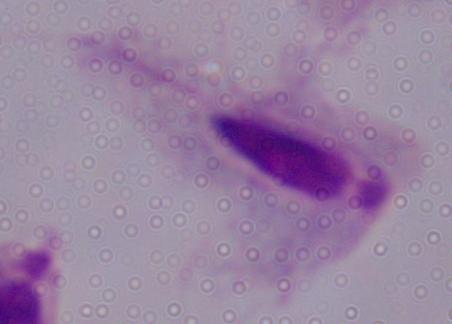
1000x magnification. Photomicrograph. A trichomonad is seen.